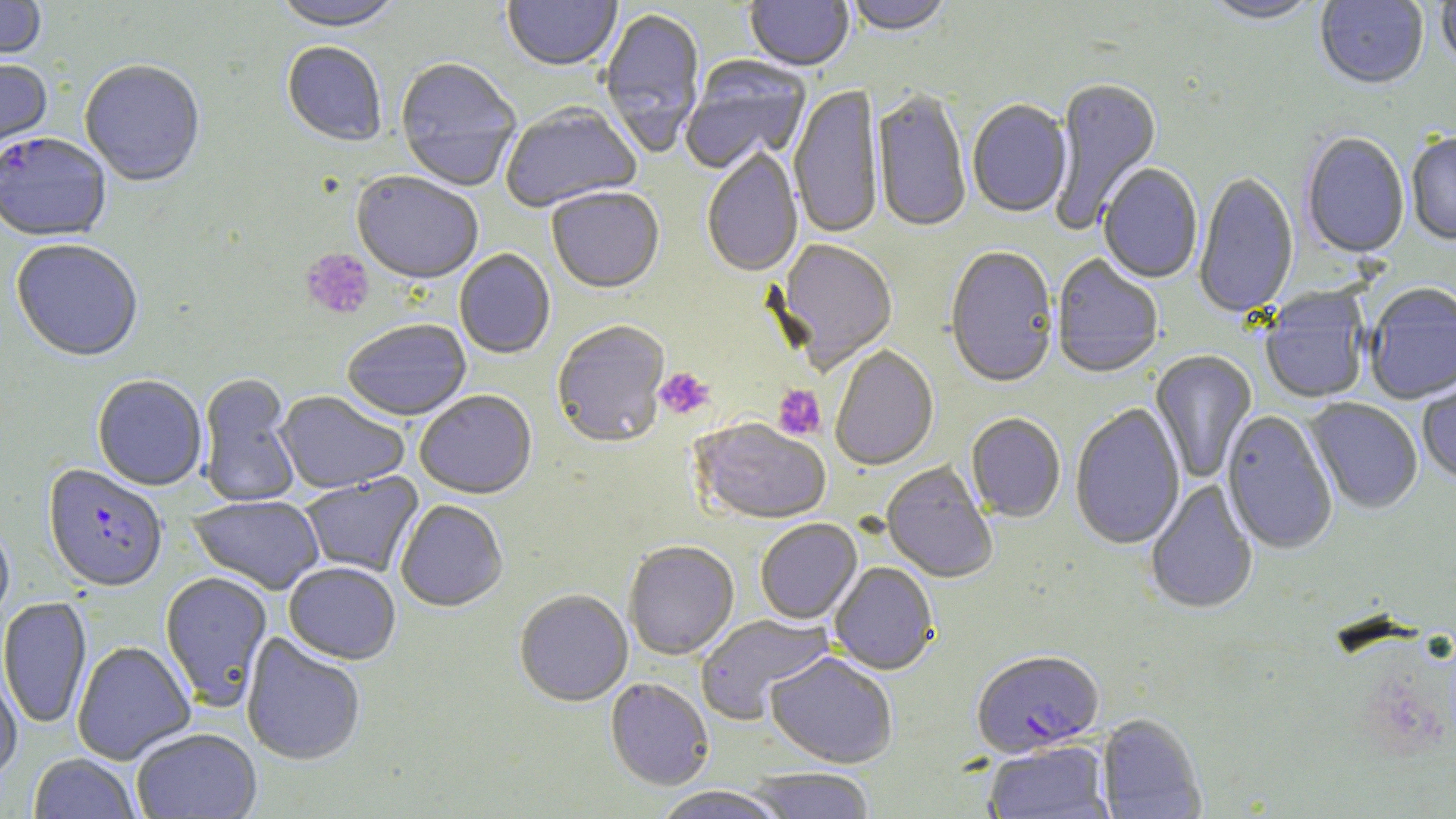 Approximate bounding boxes as named x1/y1/x2/y2 corners in pixels. Platelet locations: (x1=300, y1=248, x2=375, y2=320), (x1=654, y1=367, x2=715, y2=420), (x1=773, y1=385, x2=826, y2=441). Uninfected red blood cell locations: (x1=0, y1=0, x2=46, y2=65), (x1=272, y1=0, x2=402, y2=34), (x1=845, y1=0, x2=954, y2=38), (x1=1199, y1=0, x2=1323, y2=27), (x1=502, y1=1, x2=622, y2=73), (x1=745, y1=1, x2=853, y2=73), (x1=1315, y1=1, x2=1429, y2=91), (x1=1436, y1=1, x2=1456, y2=72), (x1=599, y1=8, x2=706, y2=159), (x1=282, y1=43, x2=387, y2=148), (x1=681, y1=57, x2=812, y2=176), (x1=0, y1=59, x2=53, y2=158), (x1=395, y1=59, x2=521, y2=192), (x1=79, y1=62, x2=205, y2=189), (x1=1049, y1=78, x2=1163, y2=232), (x1=789, y1=84, x2=882, y2=240), (x1=872, y1=90, x2=971, y2=235), (x1=967, y1=100, x2=1072, y2=219), (x1=501, y1=105, x2=642, y2=215), (x1=1301, y1=133, x2=1410, y2=260), (x1=1406, y1=134, x2=1456, y2=246), (x1=702, y1=149, x2=803, y2=279), (x1=1099, y1=164, x2=1203, y2=285), (x1=351, y1=173, x2=483, y2=287), (x1=1194, y1=173, x2=1299, y2=320), (x1=547, y1=189, x2=664, y2=296), (x1=10, y1=240, x2=143, y2=364), (x1=774, y1=240, x2=898, y2=375), (x1=945, y1=248, x2=1059, y2=390), (x1=454, y1=250, x2=556, y2=360), (x1=1051, y1=255, x2=1163, y2=380), (x1=1365, y1=284, x2=1456, y2=406), (x1=1260, y1=289, x2=1371, y2=405), (x1=342, y1=321, x2=472, y2=423), (x1=552, y1=322, x2=670, y2=450), (x1=830, y1=347, x2=939, y2=472), (x1=1151, y1=350, x2=1257, y2=484), (x1=197, y1=374, x2=301, y2=509), (x1=1417, y1=374, x2=1456, y2=485), (x1=92, y1=377, x2=207, y2=492), (x1=415, y1=391, x2=537, y2=500), (x1=274, y1=392, x2=409, y2=495), (x1=1304, y1=398, x2=1423, y2=515), (x1=1069, y1=404, x2=1185, y2=551), (x1=1221, y1=410, x2=1337, y2=555), (x1=966, y1=414, x2=1065, y2=523), (x1=691, y1=419, x2=832, y2=525), (x1=881, y1=462, x2=998, y2=584), (x1=299, y1=472, x2=424, y2=579), (x1=1145, y1=479, x2=1258, y2=616), (x1=188, y1=496, x2=324, y2=595), (x1=395, y1=501, x2=508, y2=614), (x1=755, y1=519, x2=862, y2=625), (x1=0, y1=524, x2=15, y2=631), (x1=624, y1=542, x2=739, y2=661), (x1=284, y1=563, x2=400, y2=666), (x1=829, y1=563, x2=939, y2=676), (x1=160, y1=572, x2=273, y2=710), (x1=514, y1=591, x2=633, y2=707), (x1=0, y1=597, x2=92, y2=729), (x1=695, y1=614, x2=834, y2=725), (x1=241, y1=633, x2=366, y2=767), (x1=72, y1=641, x2=196, y2=765), (x1=765, y1=653, x2=898, y2=769), (x1=0, y1=660, x2=23, y2=783), (x1=605, y1=678, x2=714, y2=791), (x1=1097, y1=714, x2=1206, y2=819), (x1=131, y1=729, x2=262, y2=819), (x1=983, y1=741, x2=1113, y2=819), (x1=28, y1=754, x2=141, y2=818), (x1=747, y1=768, x2=875, y2=819), (x1=651, y1=787, x2=790, y2=819). Plasmodium falciparum-infected red blood cell locations: (x1=0, y1=134, x2=111, y2=244), (x1=42, y1=466, x2=168, y2=594), (x1=971, y1=651, x2=1104, y2=758). Slide-level diagnosis: Plasmodium falciparum. Image is 1456×819 pixels. Single field of view. Thin blood smear. May-Grünwald-Giemsa stain. 1000x magnification. Light microscopy.